Locate and identify every blood parasite.
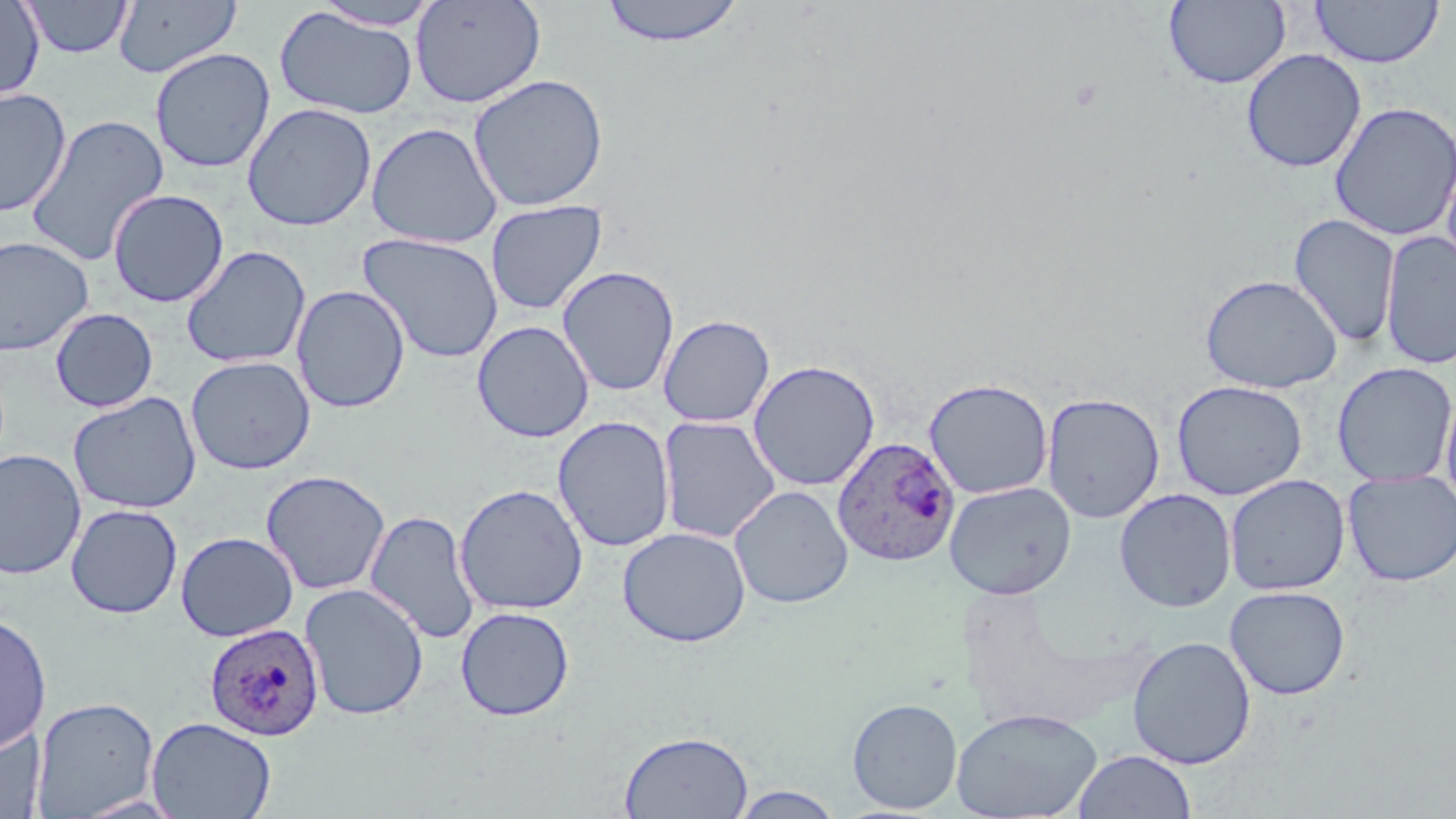

Approximate bounding boxes as (x1, y1, x2, y2) in pixels.
Plasmodium ovale-infected red blood cells: (832, 435, 960, 567), (204, 622, 325, 742).
No Plasmodium falciparum, Plasmodium malariae, Plasmodium vivax, Babesia divergens, or Trypanosoma brucei observed.

slide_level_diagnosis: Plasmodium ovale
image_size: 1456×819 pixels
uninfected_red_blood_cell_locations: 'approximate bounding boxes as (x1, y1, x2, y2) in pixels: (22, 0, 133, 59), (411, 0, 546, 108), (598, 0, 748, 47), (0, 1, 44, 101), (113, 1, 242, 78), (309, 1, 445, 31), (1164, 1, 1291, 88), (1309, 1, 1444, 68), (273, 7, 418, 119), (150, 47, 275, 173), (1241, 48, 1366, 173), (468, 74, 609, 212), (0, 87, 72, 217), (242, 102, 377, 232), (1329, 102, 1455, 241), (24, 113, 169, 269), (366, 122, 503, 249), (108, 189, 229, 308), (485, 200, 607, 315), (1289, 213, 1400, 348), (1380, 231, 1456, 369), (357, 232, 504, 362), (0, 237, 94, 355), (181, 245, 311, 369), (557, 265, 679, 397), (1200, 274, 1342, 393), (291, 285, 411, 414), (50, 307, 158, 412), (658, 314, 775, 427), (472, 320, 594, 443), (185, 355, 316, 475), (748, 359, 880, 491), (1332, 362, 1455, 486), (923, 377, 1053, 499), (1171, 380, 1308, 500), (1440, 385, 1456, 513), (67, 391, 202, 514), (1041, 392, 1165, 523), (552, 416, 675, 552), (658, 416, 781, 543), (0, 448, 86, 580), (261, 470, 390, 595), (1342, 470, 1456, 586), (1225, 474, 1351, 596), (944, 480, 1077, 600), (454, 483, 589, 616), (729, 485, 854, 608), (1114, 489, 1236, 612), (66, 503, 183, 619), (364, 510, 481, 645), (67, 520, 300, 626), (618, 526, 751, 647), (175, 531, 299, 642), (300, 583, 429, 720), (1225, 585, 1350, 700), (455, 606, 574, 721), (0, 611, 52, 756), (1127, 635, 1256, 769), (31, 696, 159, 817), (847, 698, 963, 814), (951, 707, 1103, 819), (147, 716, 276, 819), (0, 724, 46, 818), (619, 730, 754, 819), (1072, 749, 1197, 818), (728, 786, 847, 819)'
preparation: thin blood smear
field_of_view: single
stain: May-Grünwald-Giemsa
modality: optical microscopy
magnification: 1000x